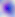
magnification = 400x
identification = Toxoplasma gondii
modality = photomicrograph